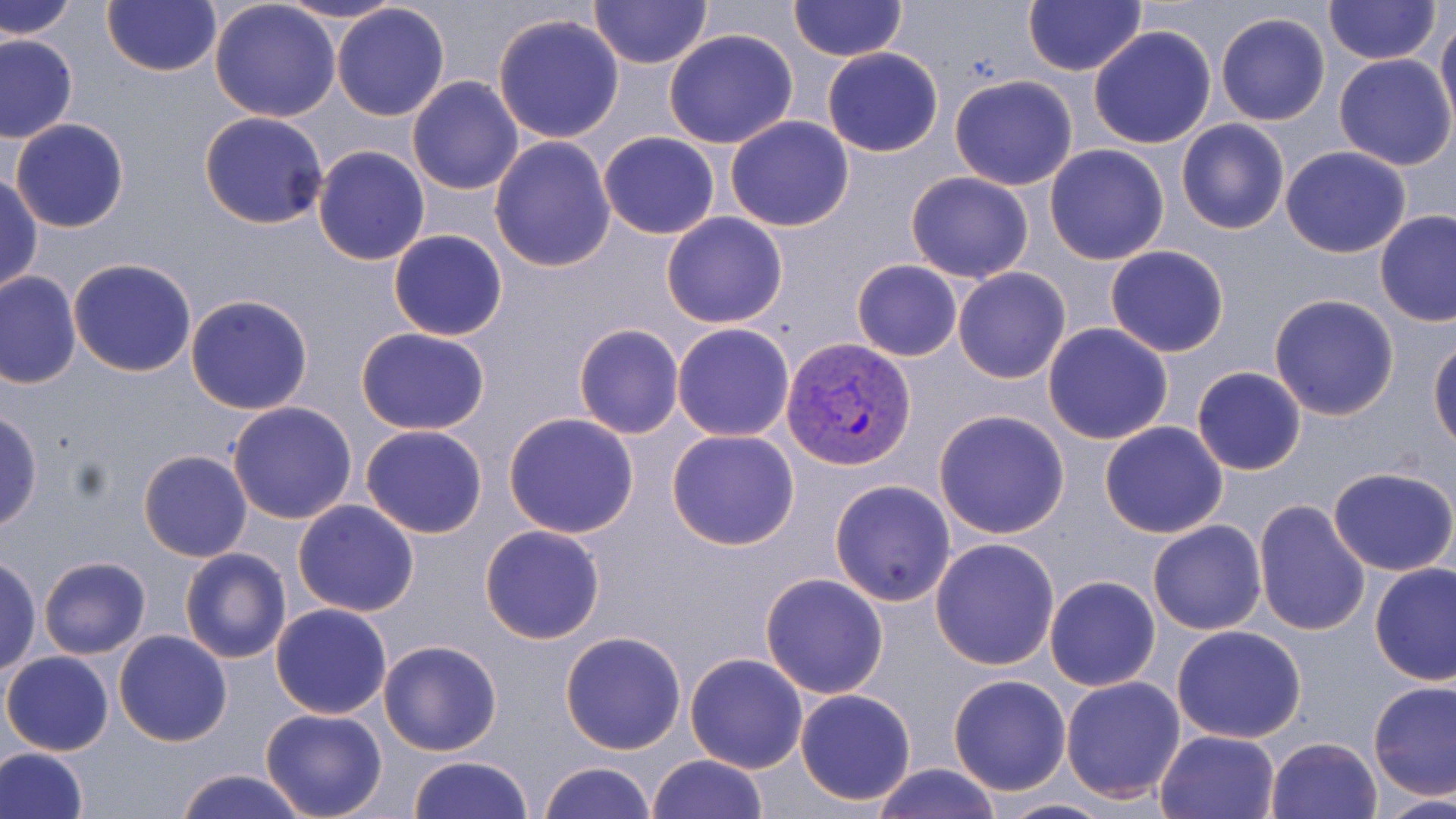

slide-level diagnosis = Plasmodium vivax
uninfected red blood cell locations = approximate bounding boxes as [x1, y1, x2, y2] in pixels: [1, 0, 80, 41], [101, 0, 221, 76], [210, 0, 341, 123], [277, 0, 408, 26], [587, 0, 712, 69], [787, 0, 907, 63], [1023, 0, 1148, 77], [1323, 0, 1440, 65], [331, 2, 451, 120], [1215, 11, 1330, 126], [493, 13, 625, 142], [1436, 15, 1456, 128], [1088, 26, 1218, 149], [664, 29, 799, 148], [0, 32, 78, 142], [822, 47, 943, 157], [1333, 54, 1455, 171], [407, 75, 524, 194], [949, 75, 1078, 191], [199, 111, 328, 229], [724, 115, 854, 233], [10, 118, 129, 233], [1177, 119, 1290, 235], [598, 131, 721, 240], [489, 137, 616, 272], [312, 145, 431, 264], [1043, 145, 1169, 264], [1281, 146, 1412, 258], [904, 172, 1034, 282], [0, 173, 43, 295], [1374, 209, 1456, 326], [660, 212, 789, 328], [388, 229, 508, 341], [1105, 244, 1230, 358], [68, 258, 197, 378], [851, 260, 962, 362], [953, 267, 1071, 384], [0, 271, 81, 389], [185, 293, 314, 414], [1268, 294, 1400, 421], [573, 323, 684, 438], [672, 323, 796, 441], [1043, 323, 1173, 444], [356, 327, 490, 434], [1430, 340, 1456, 451], [1192, 366, 1306, 475], [227, 401, 358, 524], [1, 408, 41, 532], [932, 409, 1071, 539], [503, 412, 639, 538], [1100, 420, 1229, 539], [360, 425, 488, 538], [667, 429, 801, 549], [139, 449, 252, 562], [1329, 468, 1456, 576], [830, 479, 958, 606], [1253, 496, 1371, 636], [293, 500, 420, 618], [1148, 520, 1266, 635], [479, 525, 605, 645], [930, 537, 1059, 669], [180, 547, 291, 664], [0, 557, 41, 679], [39, 557, 151, 659], [1369, 563, 1455, 685], [760, 573, 891, 698], [1044, 575, 1161, 691], [269, 603, 393, 719], [1172, 625, 1306, 744], [114, 630, 233, 746], [559, 631, 688, 755], [377, 639, 504, 756], [2, 651, 113, 755], [684, 652, 809, 772], [948, 674, 1071, 794], [1060, 677, 1187, 802], [1368, 681, 1456, 800], [794, 688, 918, 805], [259, 707, 388, 819], [1156, 729, 1280, 818], [1266, 736, 1382, 819], [0, 747, 88, 819], [646, 753, 768, 819], [407, 755, 534, 819], [538, 760, 656, 819], [867, 763, 1005, 819], [172, 769, 310, 819], [1374, 793, 1456, 819], [984, 797, 1119, 818]
preparation = thin blood smear
magnification = 1000x
field of view = single
image size = 1456×819 pixels
Plasmodium vivax-infected red blood cell locations = approximate bounding boxes as [x1, y1, x2, y2] in pixels: [781, 336, 915, 470]
stain = May-Grünwald-Giemsa
modality = light microscopy